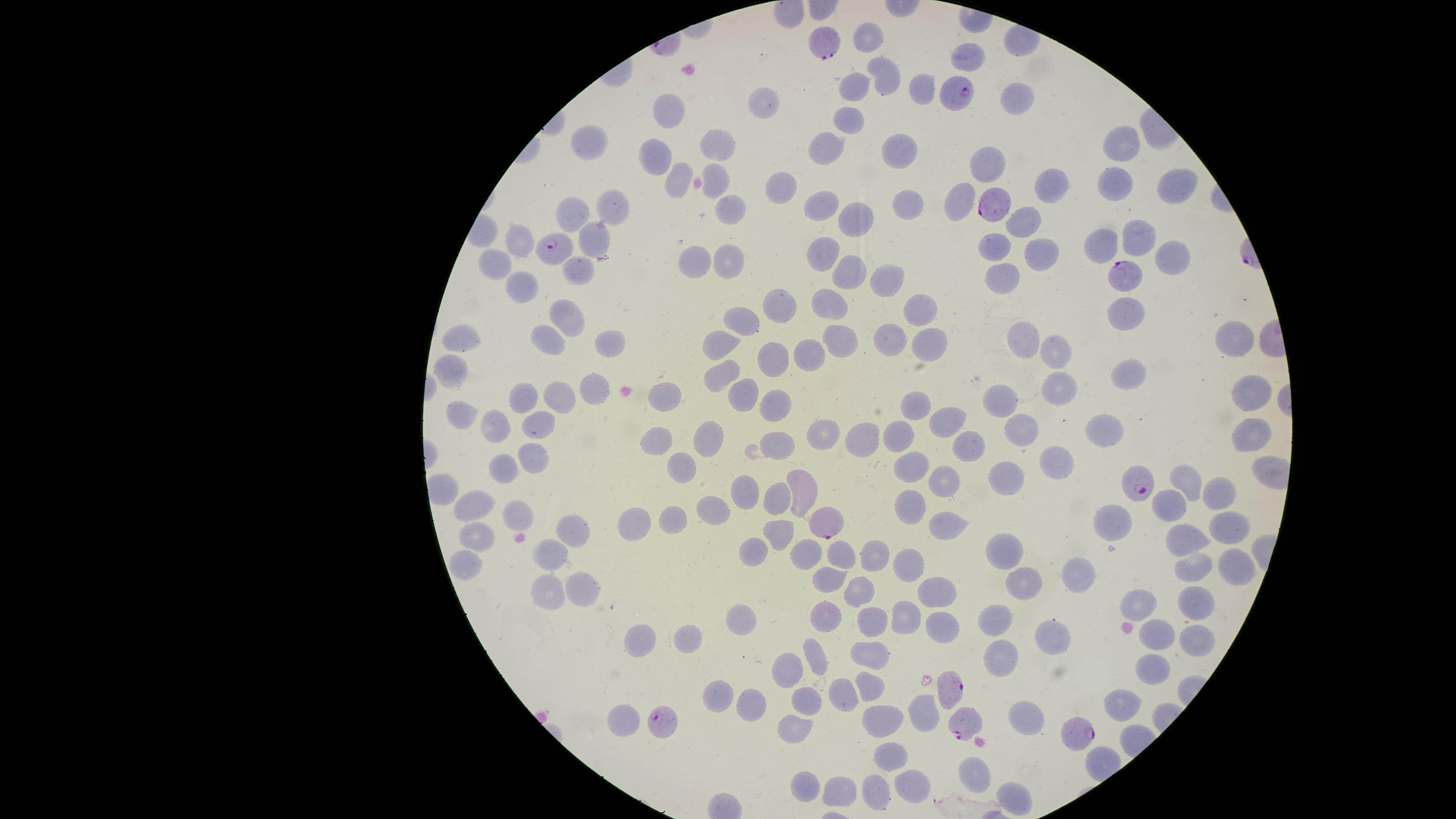
Approximate marker points as (x, y) in pixels. Parasitized RBCs: (830, 49), (956, 94), (992, 205), (557, 251), (1121, 276), (1135, 479), (826, 524), (954, 687), (665, 722), (963, 722), (1081, 733). Uninfected RBCs: (870, 36), (966, 57), (890, 78), (858, 86), (922, 89), (1015, 97), (764, 98), (668, 115), (849, 120), (828, 142), (1125, 142), (720, 144), (590, 145), (894, 148), (657, 159), (988, 162), (717, 175), (676, 178), (1115, 183), (781, 187), (1052, 187), (1176, 187), (905, 199), (615, 200), (963, 201), (821, 204), (569, 211), (730, 212), (857, 220), (1020, 222), (1139, 236), (588, 237), (519, 244), (1103, 244), (995, 246), (1042, 251), (822, 253), (729, 258), (1167, 258), (692, 260), (497, 261), (575, 270), (847, 273), (889, 274), (1006, 278), (524, 285), (781, 305), (831, 308), (919, 308), (1125, 314), (569, 315), (745, 321), (1020, 337), (458, 338), (1230, 338), (548, 339), (610, 340), (890, 341), (841, 342), (722, 343), (924, 343), (1057, 353), (808, 355), (771, 360), (454, 369), (723, 375), (1126, 378), (589, 388), (1252, 389), (661, 391), (741, 391), (1060, 391), (521, 397), (773, 400), (563, 401), (1002, 404), (914, 405), (464, 418), (946, 420), (534, 423), (498, 426), (1025, 429), (902, 432), (1103, 432), (1254, 432), (706, 436), (828, 436), (659, 439), (861, 441), (781, 442), (534, 455), (1055, 461), (684, 465), (500, 468), (912, 468), (1011, 480), (944, 481), (1185, 481), (744, 492), (805, 493), (777, 495), (1217, 496), (1170, 500), (472, 506), (908, 506), (718, 509), (675, 512), (518, 515), (1117, 519), (635, 521), (1229, 528), (571, 529), (948, 531), (775, 537), (1190, 537), (479, 540), (1007, 546), (750, 551), (809, 551), (845, 551), (551, 553), (873, 553), (466, 560), (904, 562), (1237, 564), (1189, 567), (1076, 573), (829, 577), (1020, 585), (586, 587), (857, 590), (937, 591), (550, 594), (1142, 602), (1196, 604), (908, 612), (740, 613), (831, 613), (874, 619), (998, 620), (939, 628), (689, 634), (1155, 634), (1055, 635), (642, 637), (1194, 640), (816, 656), (876, 656), (1002, 660), (791, 668), (1148, 669), (868, 685), (845, 691), (723, 698), (803, 700), (752, 704), (1124, 706), (924, 709), (624, 714), (889, 715), (1023, 715), (794, 731), (891, 755), (978, 772), (807, 786), (913, 787), (843, 794), (873, 796), (1013, 802). Circular visible region. Smartphone photograph through the microscope eyepiece. Thin smear of blood. Single field of view. Species: Plasmodium falciparum. Giemsa-stained preparation. Presence: malaria parasites seen. Image is 1456×819 pixels.